Describe the morphology of the red blood cells.
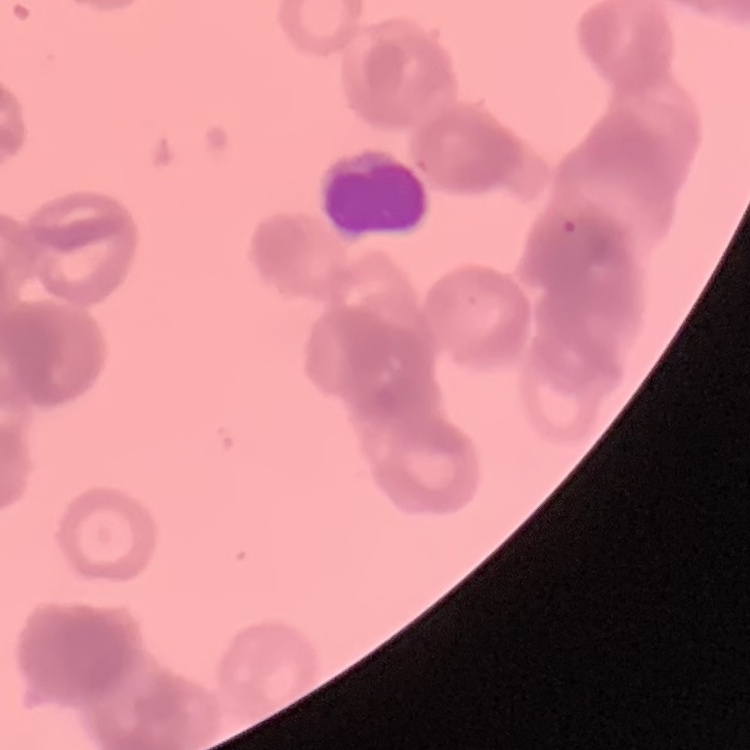
They show rouleaux formation.

stain = Field's or Giemsa
preparation = thin blood smear
image type = square crop of a larger photomicrograph